Identify the blood parasite species.
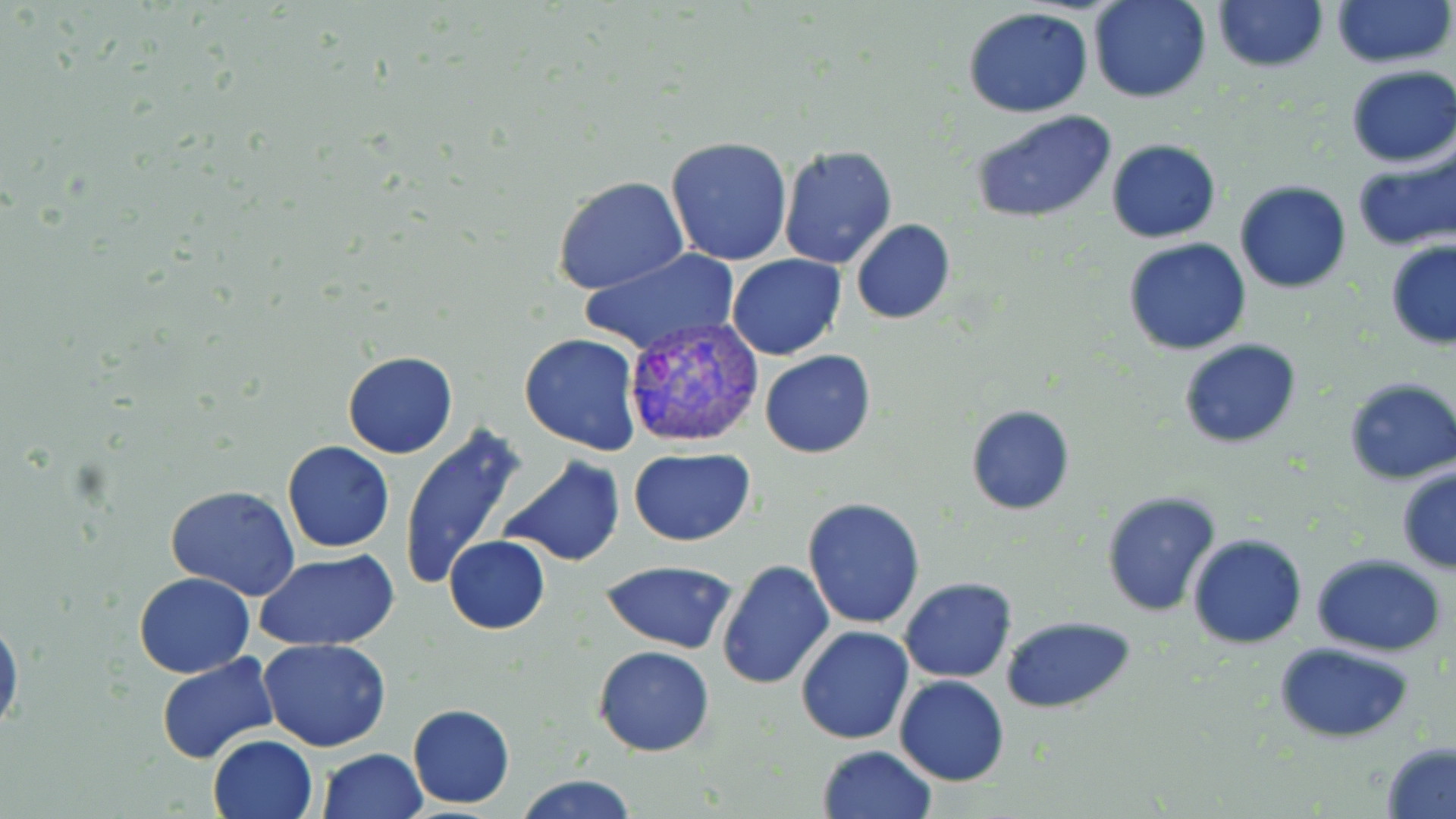
Plasmodium vivax.

Approximate bounding boxes as named x1/y1/x2/y2 corners in pixels. Plasmodium vivax-infected red blood cell locations: (x1=626, y1=313, x2=766, y2=449). Uninfected red blood cell locations: (x1=1088, y1=0, x2=1213, y2=104), (x1=1212, y1=0, x2=1328, y2=72), (x1=1331, y1=0, x2=1453, y2=71), (x1=963, y1=8, x2=1094, y2=117), (x1=1345, y1=67, x2=1456, y2=167), (x1=970, y1=109, x2=1117, y2=225), (x1=664, y1=136, x2=794, y2=266), (x1=1105, y1=138, x2=1222, y2=241), (x1=777, y1=144, x2=898, y2=269), (x1=1352, y1=146, x2=1456, y2=253), (x1=552, y1=176, x2=690, y2=295), (x1=1234, y1=180, x2=1353, y2=294), (x1=850, y1=219, x2=956, y2=324), (x1=1122, y1=237, x2=1252, y2=356), (x1=1385, y1=240, x2=1456, y2=348), (x1=577, y1=247, x2=741, y2=357), (x1=727, y1=254, x2=847, y2=360), (x1=519, y1=333, x2=643, y2=456), (x1=1177, y1=338, x2=1301, y2=449), (x1=759, y1=350, x2=876, y2=459), (x1=342, y1=352, x2=457, y2=459), (x1=1341, y1=378, x2=1456, y2=485), (x1=966, y1=405, x2=1075, y2=515), (x1=401, y1=428, x2=528, y2=590), (x1=282, y1=441, x2=394, y2=553), (x1=628, y1=448, x2=757, y2=545), (x1=496, y1=456, x2=628, y2=568), (x1=1396, y1=467, x2=1456, y2=574), (x1=165, y1=485, x2=300, y2=603), (x1=1099, y1=489, x2=1222, y2=618), (x1=802, y1=498, x2=926, y2=630), (x1=1187, y1=533, x2=1308, y2=648), (x1=443, y1=536, x2=549, y2=634), (x1=256, y1=552, x2=400, y2=652), (x1=1310, y1=553, x2=1447, y2=657), (x1=600, y1=560, x2=738, y2=653), (x1=716, y1=560, x2=835, y2=688), (x1=134, y1=572, x2=255, y2=676), (x1=900, y1=576, x2=1017, y2=682), (x1=1000, y1=615, x2=1136, y2=713), (x1=0, y1=617, x2=23, y2=739), (x1=796, y1=625, x2=915, y2=745), (x1=258, y1=640, x2=389, y2=753), (x1=1274, y1=642, x2=1417, y2=743), (x1=592, y1=646, x2=715, y2=758), (x1=155, y1=652, x2=280, y2=766), (x1=895, y1=675, x2=1010, y2=786), (x1=406, y1=702, x2=515, y2=808), (x1=208, y1=735, x2=319, y2=819), (x1=1380, y1=742, x2=1456, y2=818), (x1=816, y1=744, x2=938, y2=819), (x1=317, y1=748, x2=428, y2=819), (x1=515, y1=773, x2=637, y2=819). 1000x magnification. One field of a larger specimen. Image is 1456×819 pixels. Light microscopy. May-Grünwald-Giemsa stain. Thin blood smear.